State which parasite is depicted.
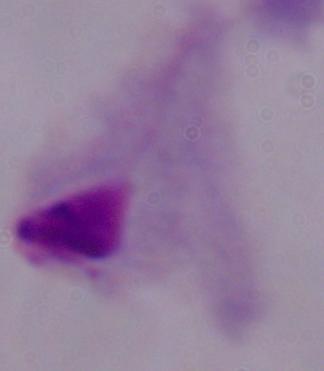

A trichomonad.

magnification = 1000x
modality = photomicrograph